Outline each blood parasite and name the species.
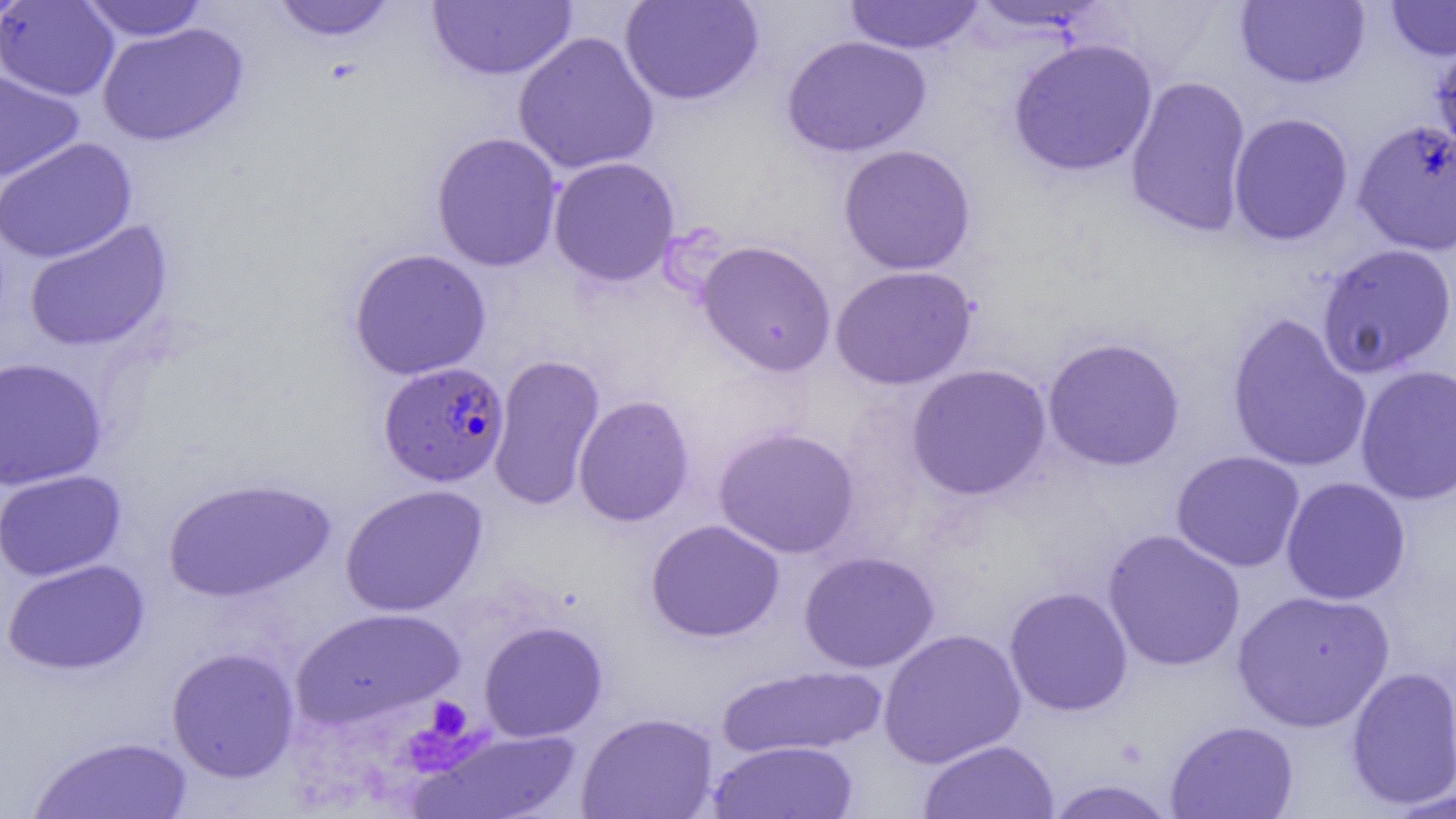
Approximate bounding boxes as [x1, y1, x2, y2] in pixels.
Plasmodium falciparum-infected red blood cells: [379, 361, 510, 486].
No Plasmodium ovale, Plasmodium malariae, Plasmodium vivax, Babesia divergens, or Trypanosoma brucei observed.

Platelet locations: [418, 696, 476, 746], [400, 708, 477, 778]. Uninfected red blood cell locations: [0, 0, 33, 26], [269, 0, 398, 42], [620, 0, 763, 106], [843, 0, 985, 54], [1384, 0, 1456, 61], [0, 1, 119, 101], [78, 1, 210, 41], [428, 1, 576, 81], [963, 1, 1111, 35], [1235, 1, 1370, 89], [96, 22, 249, 147], [512, 31, 660, 175], [1429, 33, 1456, 167], [781, 35, 932, 157], [1008, 37, 1158, 177], [0, 69, 84, 183], [1124, 74, 1253, 238], [1228, 112, 1354, 245], [1352, 118, 1456, 256], [430, 131, 563, 272], [0, 137, 137, 264], [838, 144, 977, 275], [548, 156, 680, 286], [23, 218, 173, 352], [696, 239, 836, 376], [1316, 243, 1456, 379], [348, 248, 491, 380], [830, 264, 978, 390], [1226, 312, 1372, 473], [1042, 336, 1186, 472], [487, 353, 605, 511], [0, 356, 107, 491], [1355, 363, 1456, 506], [906, 364, 1052, 501], [573, 395, 694, 527], [713, 425, 860, 559], [1170, 450, 1306, 572], [0, 469, 126, 582], [161, 476, 337, 602], [1280, 476, 1411, 605], [340, 484, 488, 617], [645, 519, 785, 642], [1102, 529, 1246, 672], [798, 550, 940, 673], [2, 558, 150, 675], [1004, 586, 1133, 716], [1232, 589, 1396, 732], [290, 606, 463, 730], [478, 620, 608, 742], [878, 628, 1026, 768], [166, 646, 300, 782], [717, 664, 887, 759], [1344, 666, 1456, 810], [577, 711, 719, 819], [1165, 720, 1299, 819], [412, 727, 582, 819], [27, 735, 195, 818], [917, 739, 1059, 818], [708, 740, 859, 818], [1041, 779, 1180, 819], [1381, 786, 1456, 818]. Slide-level diagnosis: Plasmodium falciparum. One field of a larger specimen. Thin blood smear. Light microscopy. 1000x magnification. Image is 1456×819 pixels.